Locate and identify every blood parasite.
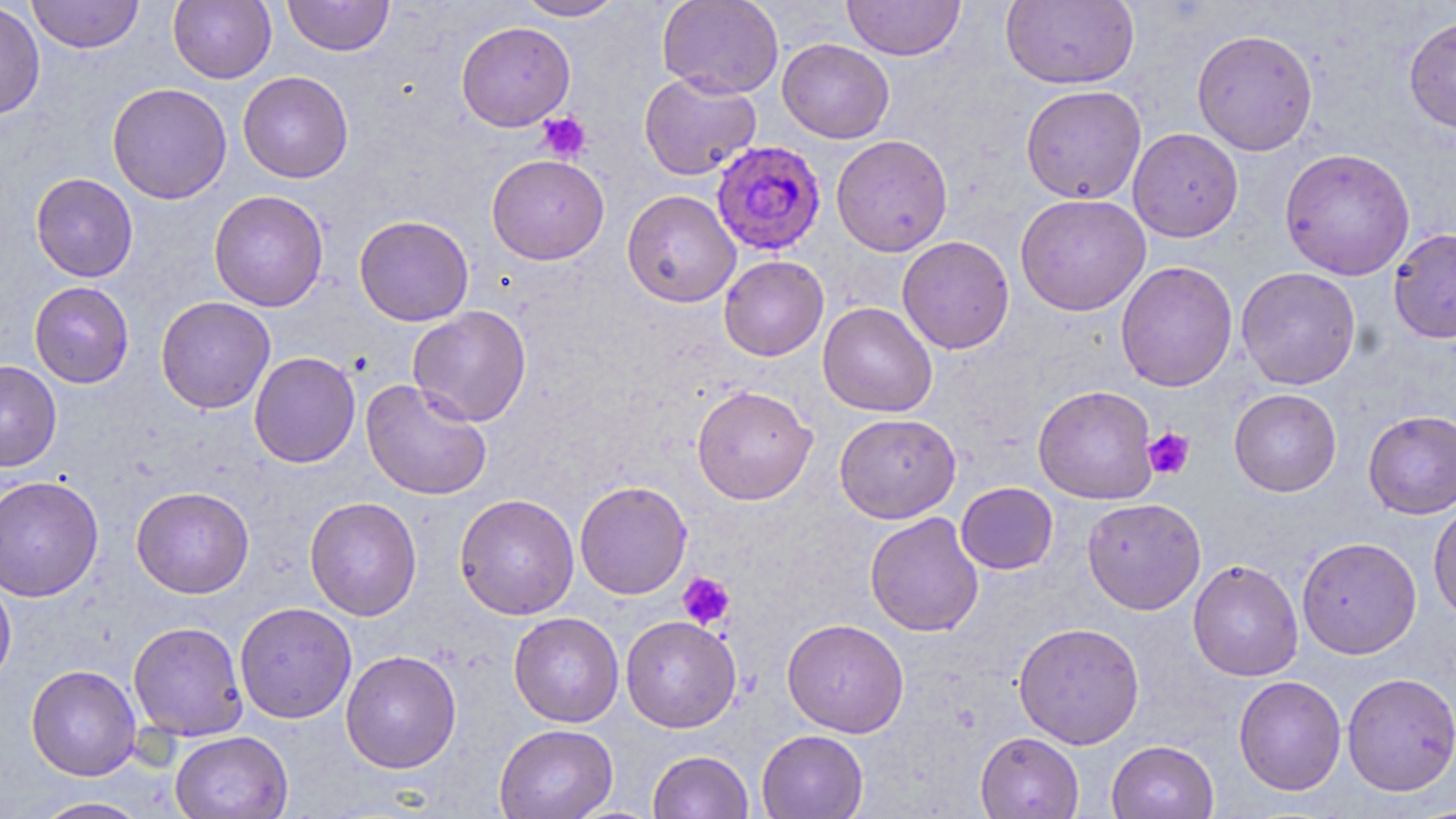

Approximate bounding boxes as named x1/y1/x2/y2 corners in pixels.
Plasmodium falciparum-infected red blood cells: (x1=711, y1=140, x2=827, y2=256).
No Plasmodium ovale, Plasmodium malariae, Plasmodium vivax, Babesia divergens, or Trypanosoma brucei observed.

Uninfected red blood cell locations: (x1=26, y1=0, x2=144, y2=53), (x1=168, y1=0, x2=276, y2=84), (x1=282, y1=0, x2=394, y2=56), (x1=514, y1=0, x2=625, y2=21), (x1=657, y1=0, x2=784, y2=98), (x1=842, y1=0, x2=966, y2=60), (x1=1001, y1=0, x2=1139, y2=89), (x1=0, y1=2, x2=46, y2=120), (x1=1403, y1=14, x2=1456, y2=134), (x1=456, y1=21, x2=575, y2=131), (x1=1191, y1=28, x2=1319, y2=156), (x1=777, y1=38, x2=894, y2=143), (x1=238, y1=71, x2=354, y2=183), (x1=639, y1=72, x2=761, y2=180), (x1=107, y1=82, x2=232, y2=204), (x1=1020, y1=85, x2=1146, y2=204), (x1=1128, y1=128, x2=1243, y2=242), (x1=831, y1=134, x2=953, y2=256), (x1=1279, y1=148, x2=1415, y2=280), (x1=487, y1=154, x2=609, y2=264), (x1=30, y1=173, x2=138, y2=282), (x1=622, y1=189, x2=741, y2=308), (x1=209, y1=190, x2=329, y2=312), (x1=1015, y1=194, x2=1151, y2=316), (x1=354, y1=215, x2=474, y2=326), (x1=1388, y1=228, x2=1456, y2=344), (x1=897, y1=235, x2=1014, y2=354), (x1=719, y1=255, x2=829, y2=361), (x1=1115, y1=260, x2=1238, y2=392), (x1=1236, y1=266, x2=1361, y2=390), (x1=29, y1=281, x2=134, y2=388), (x1=155, y1=296, x2=276, y2=414), (x1=817, y1=301, x2=938, y2=417), (x1=407, y1=305, x2=532, y2=427), (x1=249, y1=351, x2=361, y2=468), (x1=0, y1=360, x2=62, y2=472), (x1=360, y1=378, x2=492, y2=500), (x1=691, y1=384, x2=817, y2=505), (x1=1033, y1=385, x2=1159, y2=504), (x1=1229, y1=388, x2=1342, y2=496), (x1=1363, y1=410, x2=1456, y2=518), (x1=834, y1=413, x2=961, y2=523), (x1=0, y1=475, x2=104, y2=602), (x1=574, y1=480, x2=692, y2=599), (x1=956, y1=482, x2=1058, y2=574), (x1=131, y1=486, x2=254, y2=599), (x1=454, y1=493, x2=579, y2=620), (x1=304, y1=496, x2=422, y2=621), (x1=1081, y1=498, x2=1206, y2=615), (x1=1428, y1=499, x2=1456, y2=625), (x1=864, y1=512, x2=984, y2=637), (x1=1296, y1=536, x2=1421, y2=659), (x1=1188, y1=559, x2=1304, y2=681), (x1=0, y1=573, x2=16, y2=691), (x1=234, y1=602, x2=357, y2=723), (x1=509, y1=612, x2=624, y2=727), (x1=621, y1=615, x2=741, y2=732), (x1=781, y1=618, x2=909, y2=737), (x1=128, y1=621, x2=248, y2=741), (x1=1013, y1=622, x2=1145, y2=749), (x1=340, y1=649, x2=462, y2=773), (x1=26, y1=665, x2=142, y2=780), (x1=1341, y1=672, x2=1456, y2=796), (x1=1233, y1=675, x2=1346, y2=795), (x1=494, y1=723, x2=618, y2=819), (x1=169, y1=730, x2=292, y2=819), (x1=756, y1=730, x2=869, y2=819), (x1=975, y1=731, x2=1084, y2=819), (x1=1106, y1=740, x2=1219, y2=819), (x1=647, y1=750, x2=754, y2=819), (x1=30, y1=797, x2=154, y2=818). Platelet locations: (x1=537, y1=111, x2=592, y2=162), (x1=1142, y1=427, x2=1195, y2=480), (x1=678, y1=572, x2=735, y2=630). Slide-level diagnosis: Plasmodium falciparum. Thin blood film. Captured at 1000x magnification. May-Grünwald-Giemsa-stained preparation. Image is 1456×819 pixels. Light microscopy. Single field of view.